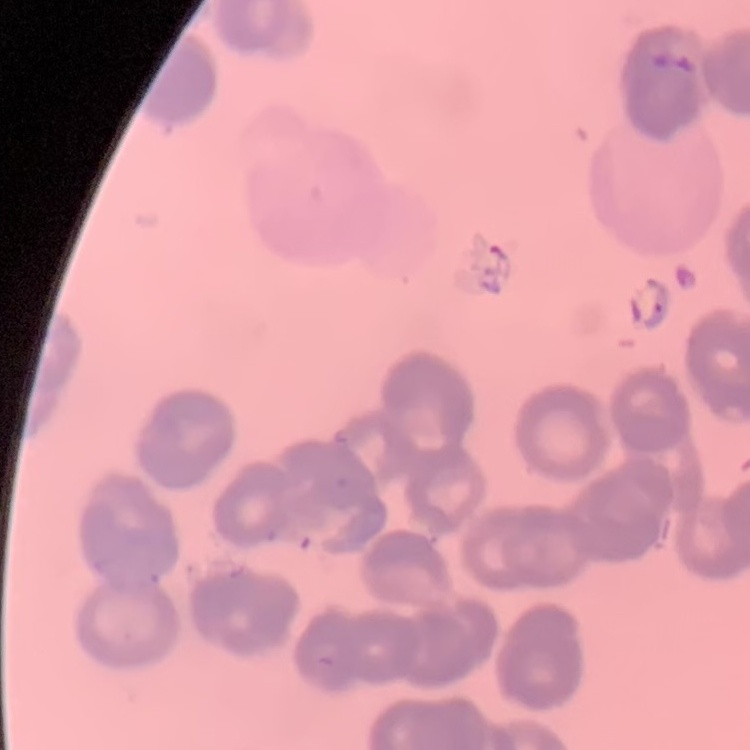 The red blood cells exhibit rouleaux formation. Thin blood smear. Square crop of a larger photomicrograph. Stained with either Field's or Giemsa.